Give the preparation type.
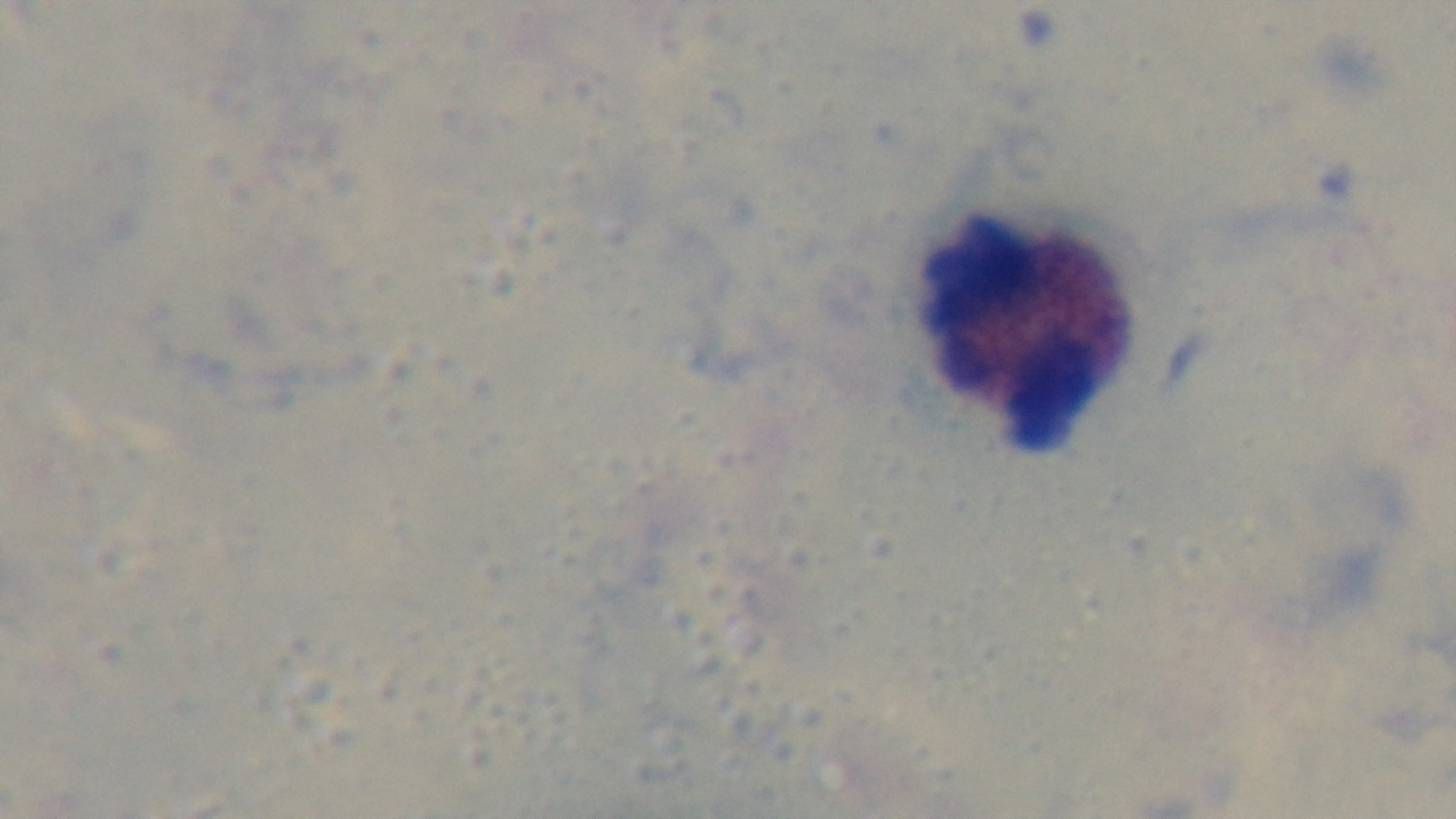
A thick smear.

{
  "malaria_status": "uninfected",
  "modality": "light microscopy",
  "objective": "100x oil immersion",
  "field_of_view": "single",
  "capture": "mounted 4K digital camera",
  "stain": "Giemsa"
}